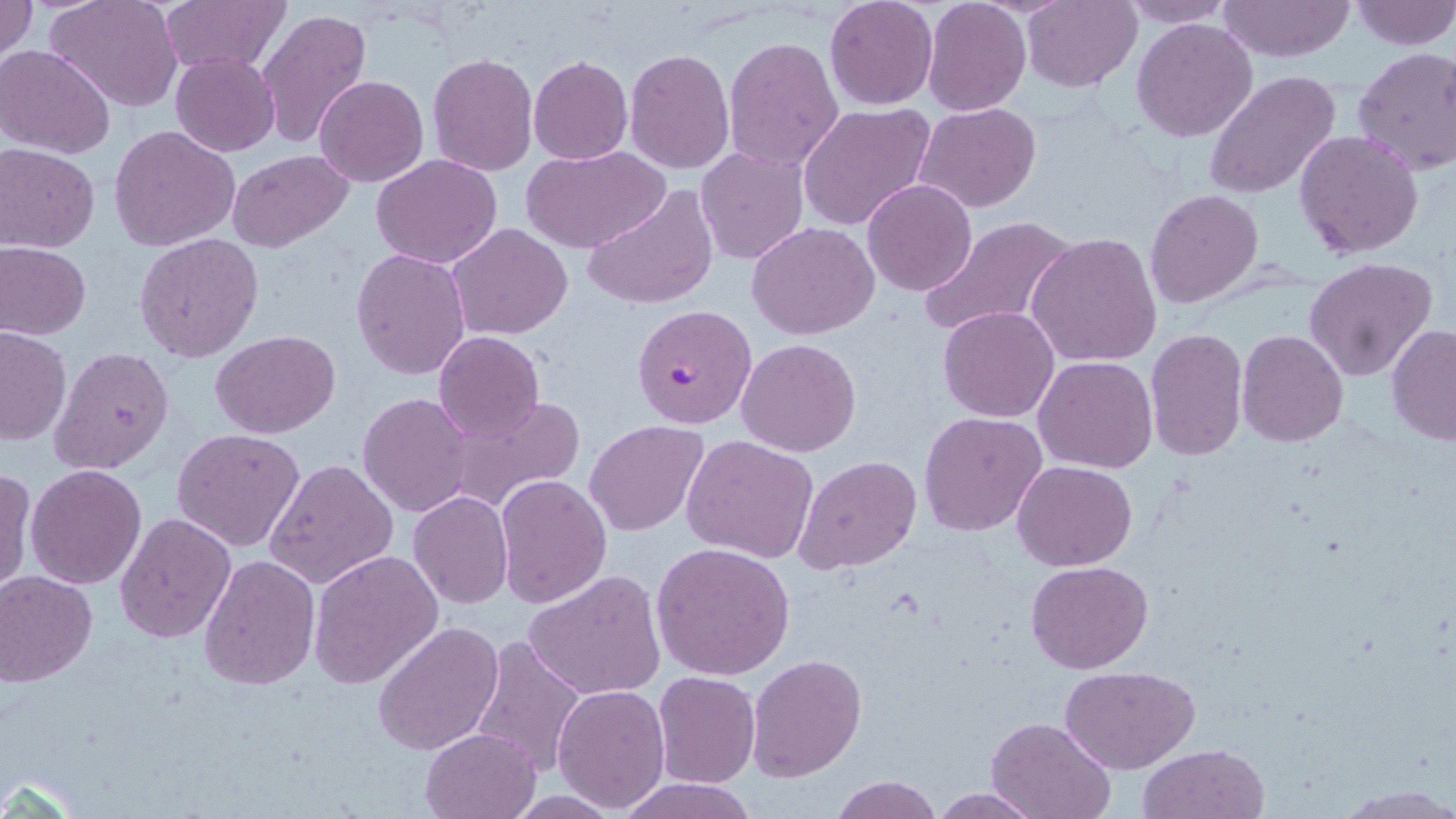 Approximate bounding boxes as [x1, y1, x2, y2] in pixels. Uninfected red blood cell locations: [0, 0, 38, 64], [47, 0, 184, 113], [161, 0, 287, 78], [824, 0, 939, 110], [922, 0, 1030, 117], [1023, 0, 1141, 92], [1117, 0, 1236, 27], [1349, 0, 1456, 49], [1219, 1, 1353, 63], [257, 9, 371, 148], [1132, 16, 1258, 142], [723, 37, 845, 176], [0, 45, 116, 159], [1351, 46, 1456, 177], [625, 48, 734, 173], [170, 51, 280, 156], [428, 53, 538, 175], [528, 56, 633, 166], [1204, 71, 1342, 199], [314, 75, 429, 187], [914, 103, 1041, 213], [798, 104, 936, 231], [109, 124, 240, 251], [1294, 129, 1423, 260], [1, 144, 100, 253], [524, 145, 670, 254], [696, 147, 809, 264], [228, 149, 356, 254], [371, 154, 502, 269], [862, 179, 977, 296], [583, 185, 717, 310], [1145, 189, 1264, 308], [919, 215, 1079, 340], [748, 222, 879, 338], [446, 223, 573, 340], [1026, 231, 1162, 368], [134, 234, 263, 361], [0, 243, 90, 339], [350, 248, 470, 380], [1303, 257, 1439, 384], [938, 306, 1058, 422], [1387, 324, 1456, 447], [0, 327, 71, 446], [1145, 329, 1249, 463], [1236, 329, 1349, 448], [211, 330, 339, 438], [432, 331, 545, 445], [737, 338, 861, 456], [51, 347, 174, 474], [1035, 355, 1158, 473], [358, 392, 475, 517], [446, 395, 582, 511], [919, 410, 1047, 538], [585, 421, 708, 535], [174, 427, 306, 551], [682, 435, 819, 563], [795, 455, 921, 574], [266, 458, 400, 590], [1013, 459, 1137, 570], [26, 464, 145, 589], [0, 467, 33, 595], [494, 475, 612, 609], [409, 491, 514, 609], [115, 513, 237, 643], [651, 542, 795, 682], [309, 549, 442, 690], [199, 554, 320, 689], [1025, 560, 1153, 674], [523, 570, 666, 701], [0, 571, 97, 685], [373, 622, 504, 758], [472, 635, 587, 780], [747, 653, 867, 780], [1058, 664, 1201, 773], [652, 672, 760, 788], [552, 685, 670, 810], [985, 716, 1114, 819], [418, 726, 543, 819], [1138, 744, 1270, 819], [830, 775, 942, 819], [615, 776, 758, 818], [1334, 786, 1455, 817], [930, 789, 1043, 818]. Plasmodium falciparum-infected red blood cell locations: [632, 303, 759, 430]. Slide-level diagnosis: Plasmodium falciparum. One field of a larger specimen. Image is 1456×819 pixels. Optical microscopy. 1000x magnification. Thin blood film. May-Grünwald-Giemsa stain.